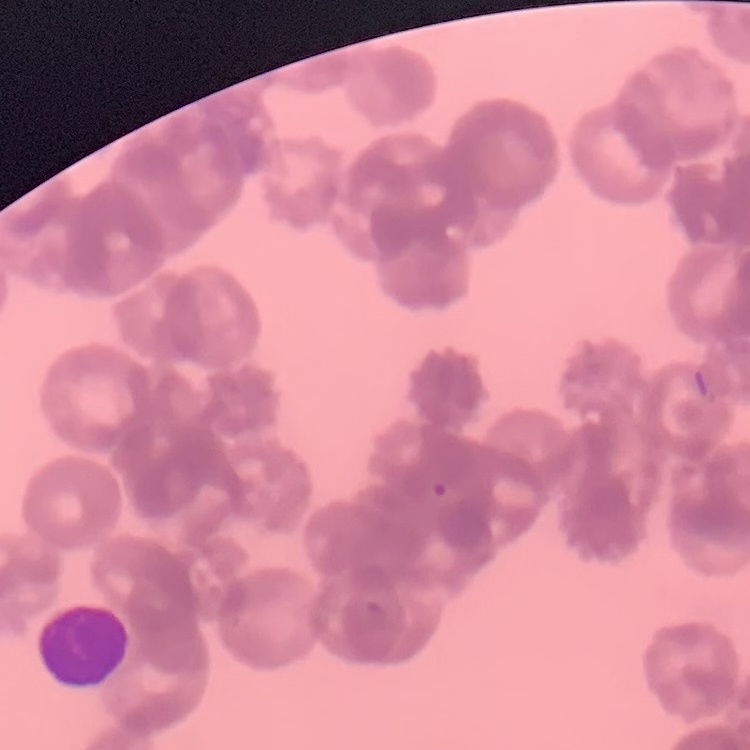
Summary:
  - Red blood cell morphology: rouleaux formation
  - Stain: Field's or Giemsa
  - Image type: square crop of a larger photomicrograph
  - Preparation: thin blood smear